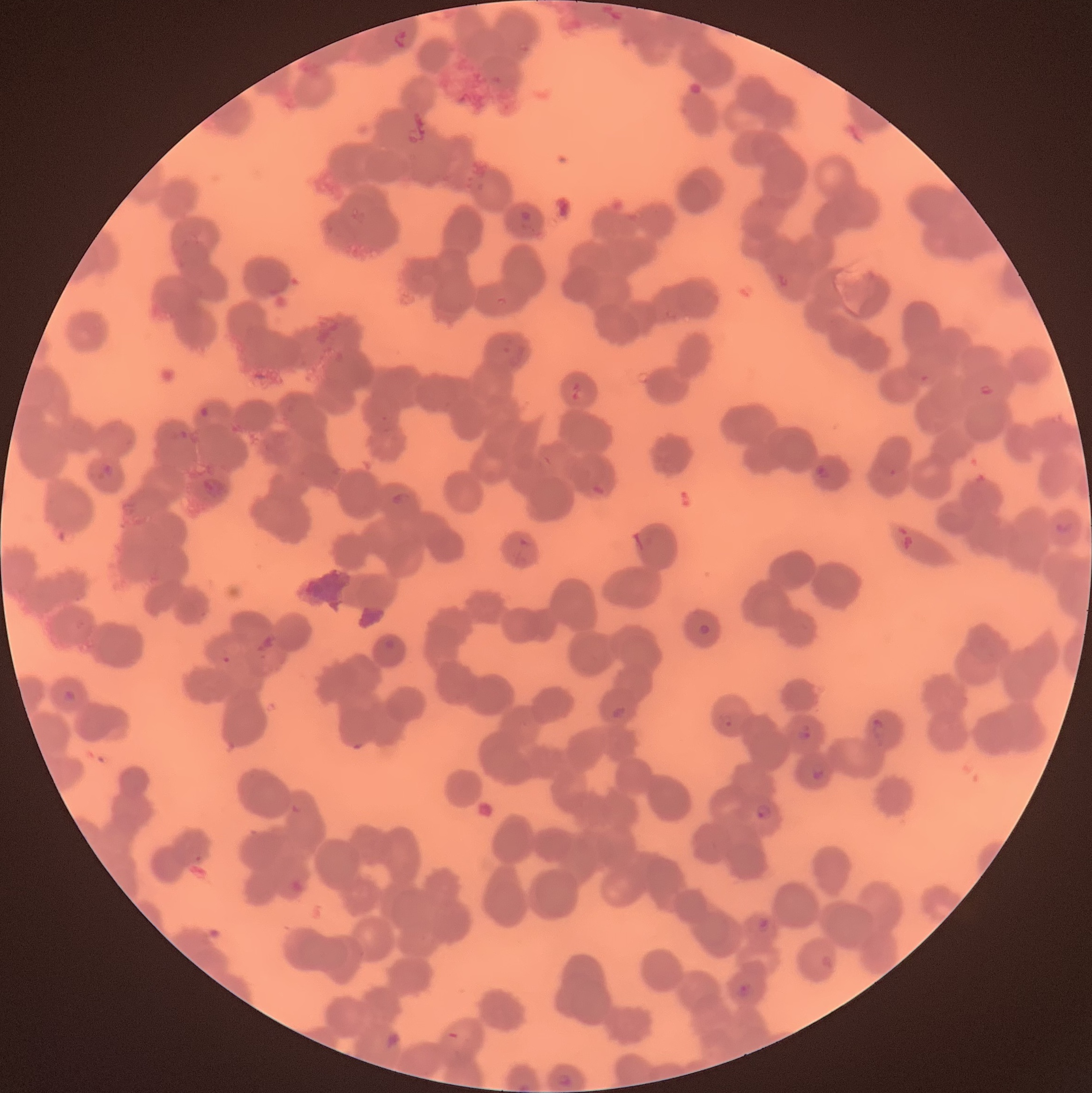
{
  "modality": "light microscopy",
  "image_size": "1092×1093 pixels",
  "plasmodium_parasite_locations": "approximate bounding boxes as named x1/y1/x2/y2 corners in pixels: (x1=392, y1=30, x2=410, y2=49), (x1=518, y1=210, x2=534, y2=230), (x1=568, y1=381, x2=583, y2=403), (x1=978, y1=383, x2=996, y2=397), (x1=197, y1=404, x2=211, y2=420), (x1=96, y1=463, x2=115, y2=480), (x1=814, y1=463, x2=833, y2=480), (x1=588, y1=478, x2=609, y2=498), (x1=391, y1=492, x2=412, y2=510), (x1=1054, y1=520, x2=1074, y2=535), (x1=697, y1=622, x2=711, y2=636), (x1=384, y1=639, x2=396, y2=651), (x1=61, y1=689, x2=79, y2=704), (x1=609, y1=706, x2=627, y2=721), (x1=716, y1=712, x2=734, y2=730), (x1=870, y1=718, x2=887, y2=746), (x1=795, y1=723, x2=814, y2=742), (x1=810, y1=764, x2=825, y2=780), (x1=291, y1=802, x2=306, y2=815), (x1=754, y1=804, x2=772, y2=821), (x1=288, y1=876, x2=311, y2=895), (x1=753, y1=917, x2=770, y2=933), (x1=735, y1=981, x2=754, y2=999), (x1=557, y1=1072, x2=573, y2=1087), (x1=516, y1=1081, x2=533, y2=1093)",
  "red_blood_cell_morphology": "rouleaux formation",
  "preparation": "thin blood smear"
}